Locate every blood parasite and identify its species.
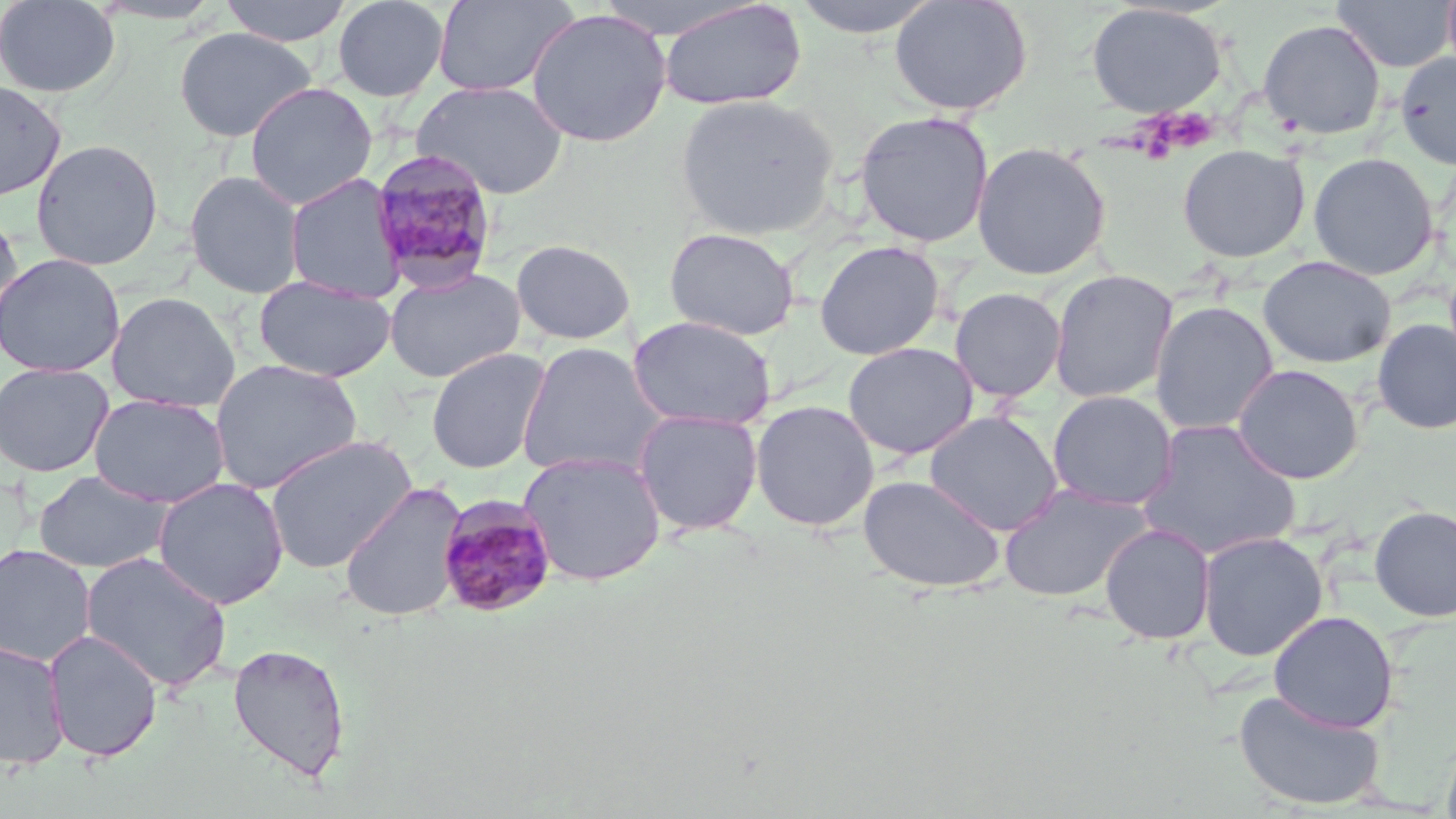

Approximate bounding boxes as named x1/y1/x2/y2 corners in pixels.
Plasmodium malariae-infected red blood cells: (x1=369, y1=149, x2=501, y2=293), (x1=436, y1=494, x2=558, y2=618).
No Plasmodium falciparum, Plasmodium ovale, Plasmodium vivax, Babesia divergens, or Trypanosoma brucei observed.

slide-level diagnosis = Plasmodium malariae
modality = light microscopy
platelet locations = approximate bounding boxes as named x1/y1/x2/y2 corners in pixels: (x1=1144, y1=108, x2=1220, y2=156)
field of view = single
stain = May-Grünwald-Giemsa
image size = 1456×819 pixels
uninfected red blood cell locations = approximate bounding boxes as named x1/y1/x2/y2 corners in pixels: (x1=0, y1=0, x2=121, y2=98), (x1=219, y1=0, x2=353, y2=47), (x1=332, y1=0, x2=449, y2=102), (x1=432, y1=0, x2=578, y2=98), (x1=789, y1=0, x2=944, y2=39), (x1=889, y1=0, x2=1032, y2=116), (x1=1332, y1=0, x2=1454, y2=72), (x1=1442, y1=0, x2=1456, y2=81), (x1=86, y1=1, x2=227, y2=26), (x1=657, y1=1, x2=807, y2=111), (x1=1086, y1=3, x2=1227, y2=119), (x1=525, y1=8, x2=672, y2=148), (x1=1257, y1=18, x2=1386, y2=140), (x1=174, y1=26, x2=316, y2=142), (x1=1394, y1=52, x2=1456, y2=169), (x1=0, y1=79, x2=67, y2=201), (x1=411, y1=80, x2=569, y2=199), (x1=244, y1=81, x2=377, y2=210), (x1=675, y1=94, x2=839, y2=240), (x1=854, y1=110, x2=994, y2=248), (x1=30, y1=139, x2=164, y2=271), (x1=971, y1=142, x2=1110, y2=280), (x1=1177, y1=144, x2=1309, y2=263), (x1=1308, y1=152, x2=1439, y2=280), (x1=184, y1=170, x2=305, y2=299), (x1=284, y1=173, x2=408, y2=304), (x1=0, y1=209, x2=25, y2=339), (x1=663, y1=227, x2=799, y2=341), (x1=510, y1=239, x2=636, y2=345), (x1=814, y1=240, x2=944, y2=360), (x1=0, y1=253, x2=124, y2=378), (x1=1258, y1=255, x2=1395, y2=368), (x1=383, y1=266, x2=526, y2=383), (x1=1049, y1=269, x2=1177, y2=404), (x1=254, y1=275, x2=395, y2=382), (x1=949, y1=287, x2=1066, y2=402), (x1=106, y1=291, x2=241, y2=413), (x1=1150, y1=300, x2=1278, y2=436), (x1=628, y1=315, x2=777, y2=430), (x1=1372, y1=319, x2=1456, y2=434), (x1=517, y1=341, x2=668, y2=480), (x1=842, y1=342, x2=978, y2=461), (x1=426, y1=347, x2=550, y2=474), (x1=209, y1=359, x2=363, y2=495), (x1=0, y1=362, x2=115, y2=478), (x1=1232, y1=364, x2=1363, y2=484), (x1=1047, y1=390, x2=1178, y2=511), (x1=90, y1=394, x2=230, y2=508), (x1=750, y1=400, x2=879, y2=532), (x1=633, y1=408, x2=763, y2=536), (x1=924, y1=410, x2=1063, y2=536), (x1=1137, y1=418, x2=1302, y2=560), (x1=263, y1=434, x2=418, y2=574), (x1=518, y1=451, x2=667, y2=586), (x1=32, y1=469, x2=172, y2=574), (x1=857, y1=474, x2=1006, y2=593), (x1=152, y1=477, x2=289, y2=609), (x1=339, y1=483, x2=467, y2=621), (x1=998, y1=484, x2=1152, y2=603), (x1=1369, y1=504, x2=1456, y2=621), (x1=1100, y1=523, x2=1217, y2=646), (x1=1197, y1=531, x2=1328, y2=660), (x1=0, y1=544, x2=97, y2=666), (x1=81, y1=551, x2=233, y2=693), (x1=1268, y1=610, x2=1399, y2=733), (x1=43, y1=629, x2=163, y2=762), (x1=0, y1=639, x2=69, y2=770), (x1=227, y1=643, x2=351, y2=782), (x1=1233, y1=688, x2=1386, y2=811)
magnification = 1000x
preparation = thin blood smear